Outline each Plasmodium falciparum parasite and classify it by life-cycle stage.
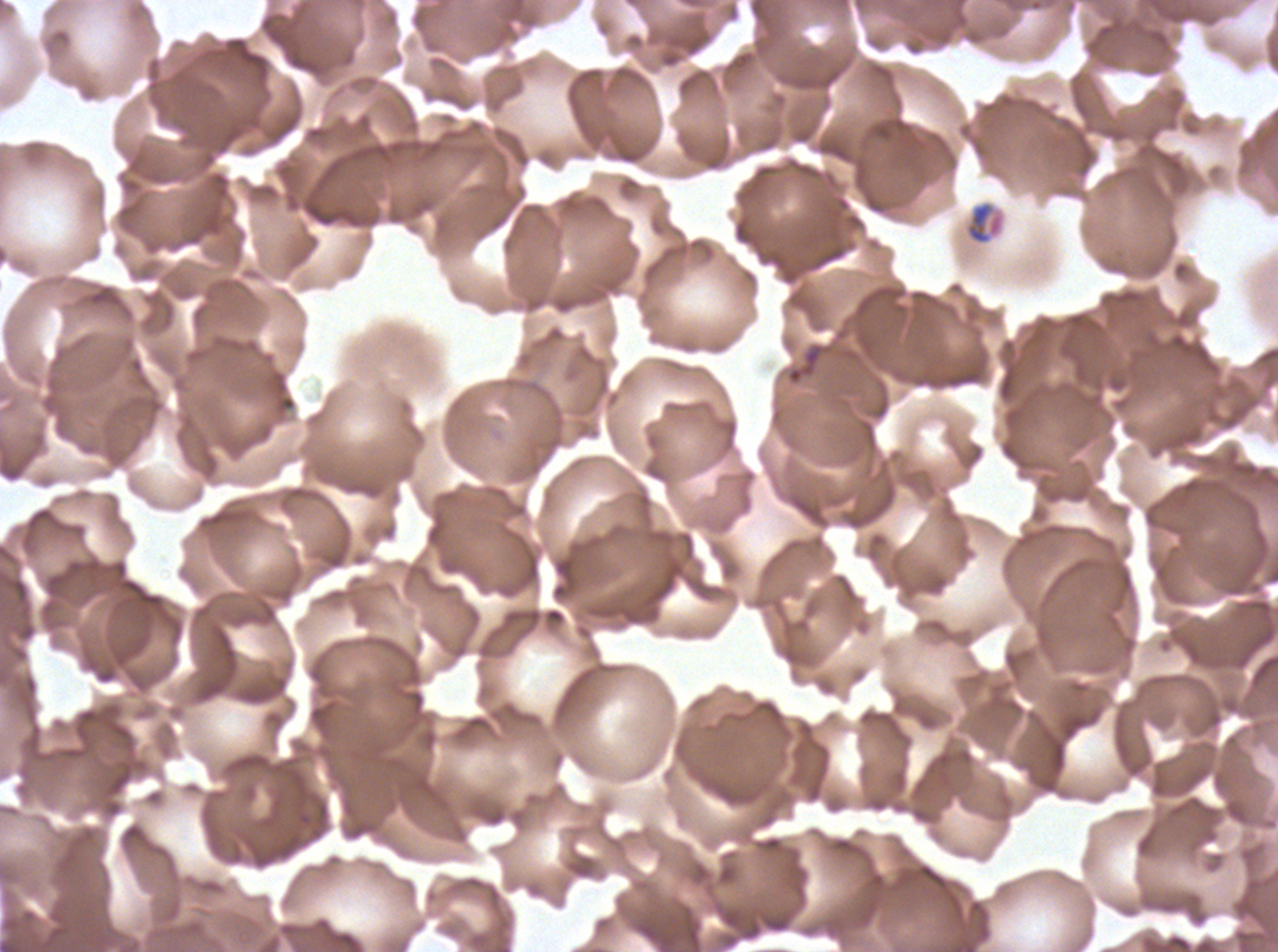

Approximate bounding boxes as (x1, y1, x2, y2) in pixels.
Late-ring/early-trophozoite forms: (964, 200, 1005, 246).
No rings, mid trophozoites, late trophozoites, early schizonts, late schizonts, segmenters, or gametocytes observed.

stain = Giemsa
image size = 1278×952 pixels
specimen = Plasmodium falciparum from a patient in The Gambia, cultured ex vivo for 24 to 48 hours
field of view = sub-image separated from a larger composite
preparation = thin blood film